Assess for parasitized red blood cells.
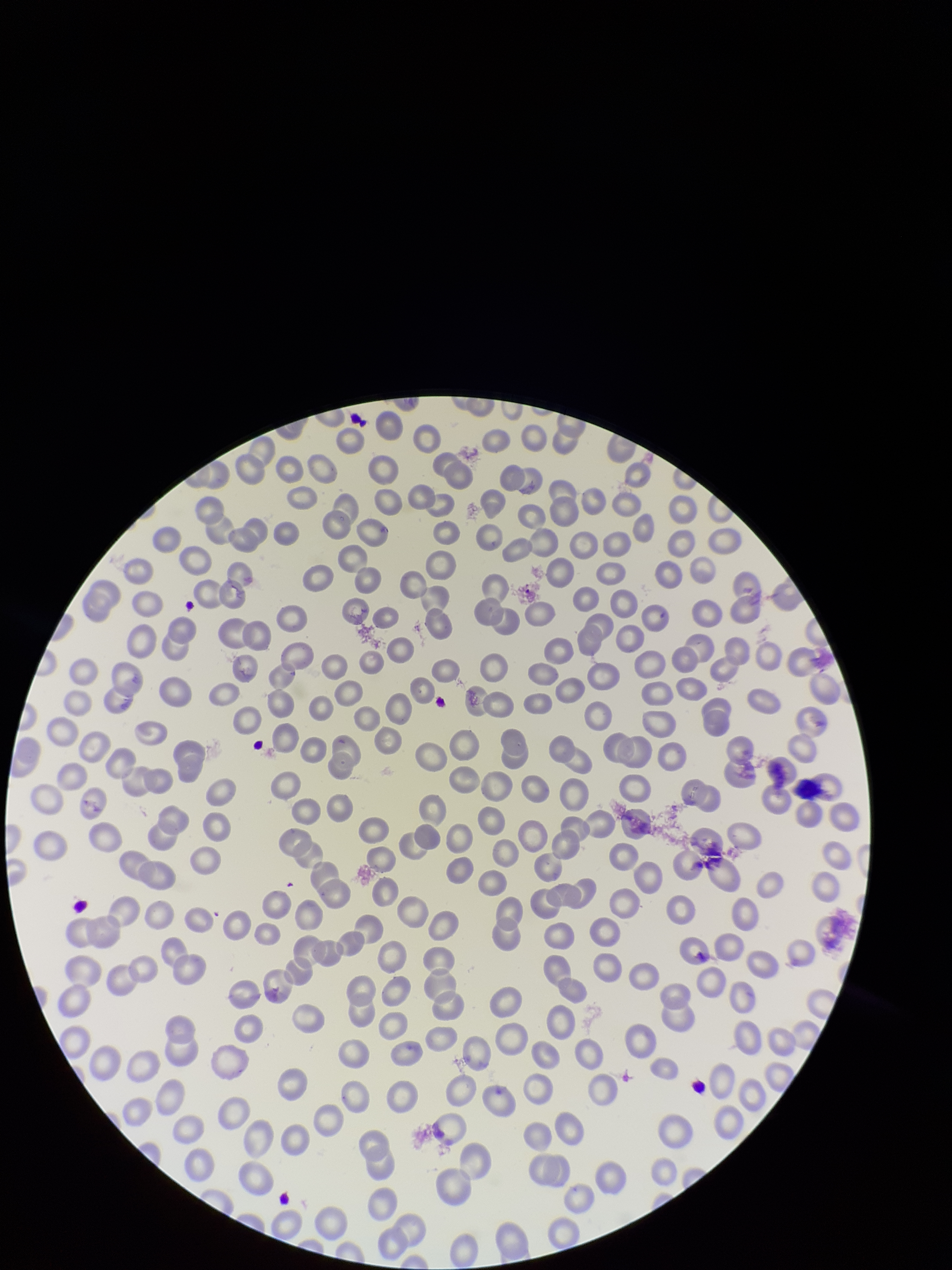

None identified.

stain: Giemsa
red_blood_cell_count: 288
field_of_view: one from this slide
image_size: 952×1270 pixels
parasitized_red_blood_cell_count: 0
patient_malaria_status: negative
preparation: thin blood smear
capture: smartphone photograph through the microscope eyepiece